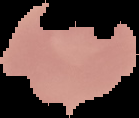 From a thin blood smear. The area outside the segmented cell region is set to black. Result: no malaria parasites seen. Image is 139×118 pixels.